Outline each Plasmodium falciparum-infected red blood cell.
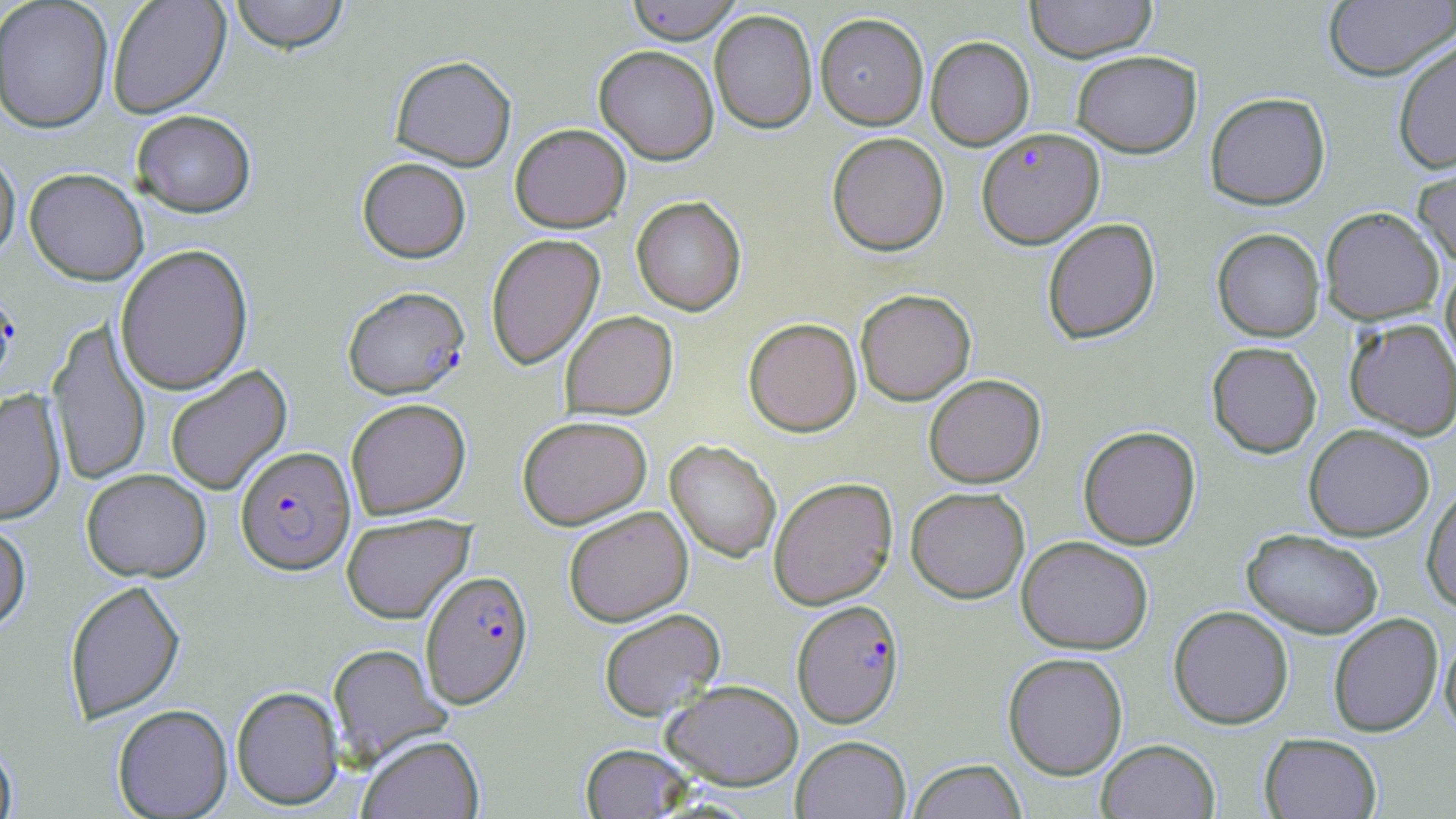

Approximate bounding boxes as (x1,y1)-(x2,y2) corner pairs in pixels.
Plasmodium falciparum-infected red blood cells: (976,127)-(1104,249), (0,284)-(20,394), (343,287)-(471,400), (235,446)-(357,576), (420,570)-(534,709), (792,599)-(904,728).

Uninfected red blood cell locations: (107,0)-(231,119), (230,0)-(349,56), (624,0)-(743,43), (1025,0)-(1156,61), (0,1)-(113,135), (1323,1)-(1456,81), (709,10)-(817,133), (815,12)-(928,129), (925,36)-(1034,149), (1392,38)-(1456,174), (594,45)-(719,165), (1071,50)-(1202,158), (390,56)-(517,172), (1205,92)-(1330,210), (131,112)-(256,220), (510,124)-(631,233), (826,132)-(949,256), (0,149)-(20,267), (1413,153)-(1456,268), (357,158)-(471,264), (24,170)-(148,287), (631,197)-(746,316), (1320,206)-(1444,325), (1042,218)-(1160,344), (1212,228)-(1325,342), (485,234)-(605,370), (115,245)-(254,396), (1440,262)-(1456,376), (855,289)-(976,405), (560,311)-(678,420), (743,317)-(862,437), (1345,317)-(1456,439), (46,318)-(151,487), (1207,341)-(1322,458), (166,365)-(292,496), (924,374)-(1046,488), (0,391)-(67,527), (345,398)-(471,520), (517,416)-(652,529), (1303,423)-(1434,541), (1078,425)-(1201,550), (665,440)-(781,562), (81,470)-(211,583), (768,476)-(897,609), (1422,484)-(1456,613), (905,486)-(1030,603), (563,506)-(693,626), (341,513)-(474,624), (0,522)-(31,635), (1242,528)-(1384,639), (1016,535)-(1154,654), (63,580)-(186,724), (1168,605)-(1294,729), (598,608)-(726,721), (1328,612)-(1443,737), (1439,631)-(1456,738), (327,643)-(453,768), (1002,652)-(1128,779), (662,679)-(803,790), (231,686)-(344,811), (113,705)-(233,818), (1259,733)-(1382,818), (357,735)-(484,819), (791,736)-(911,818), (1096,738)-(1220,819), (0,741)-(17,819), (580,744)-(694,818), (907,759)-(1028,819). Slide-level diagnosis: Plasmodium falciparum. May-Grünwald-Giemsa stain. Image is 1456×819 pixels. Thin blood smear. Captured at 1000x magnification. Light microscopy. Single field of view.